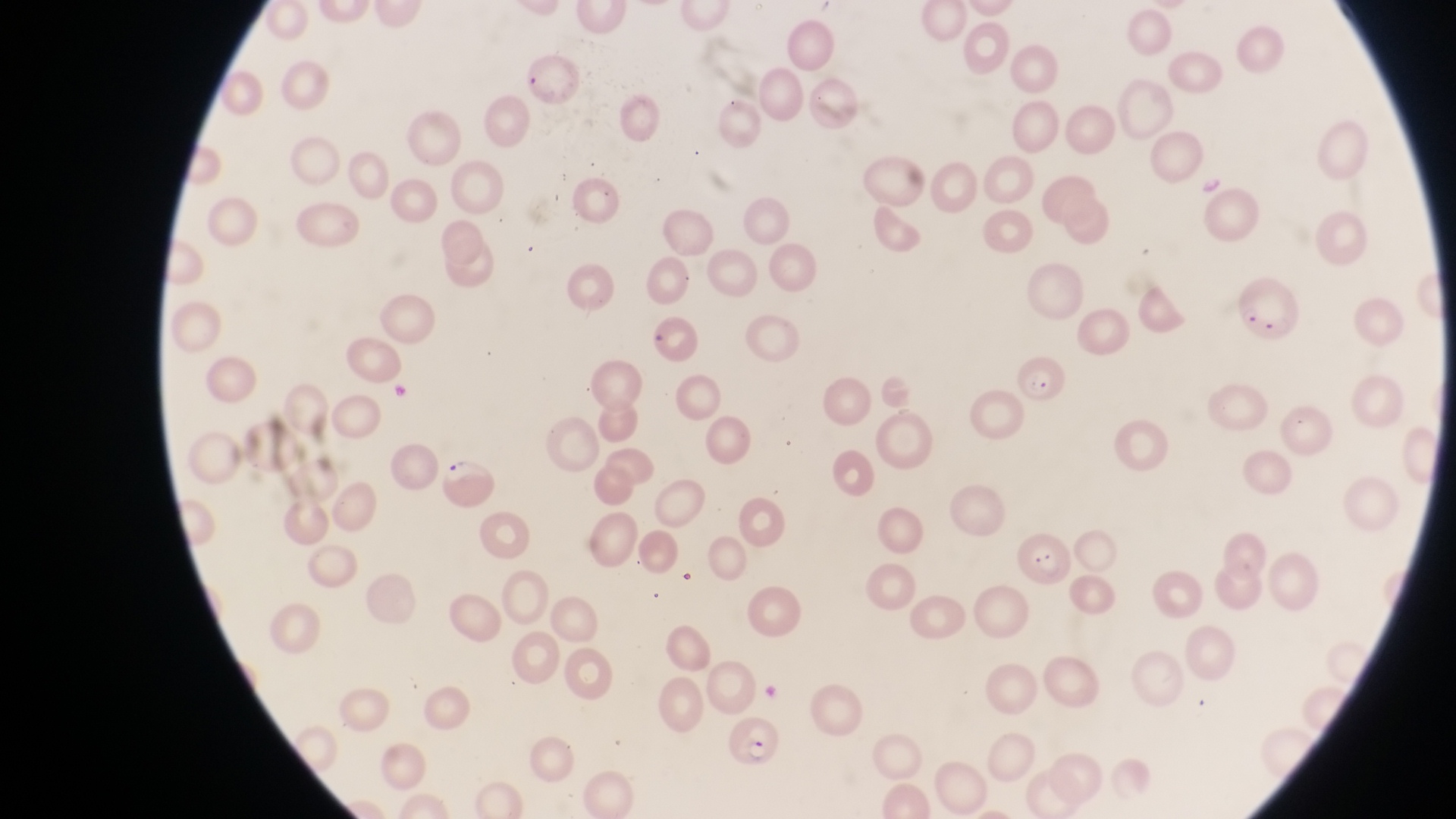
image_size: 1456×819 pixels
country: Uganda
preparation: thin blood film
capture: smartphone photograph through the eyepiece of an Olympus CX-23 microscope
artifact_platelet_like_body_stain_precipitate_or_debris_locations: 'approximate bounding boxes as {left, top, right, bottom} in pixels: {1199, 169, 1226, 198}'
parasitised_red_blood_cell_locations: 'approximate bounding boxes as {left, top, right, bottom} in pixels: {1238, 275, 1304, 346}, {1015, 356, 1070, 403}, {436, 459, 495, 511}, {720, 711, 783, 772}'
field_of_view: single
magnification: 1000x